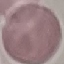 Malaria status: uninfected. Giemsa-stained preparation. Automatically extracted cell patch, resized to 64 × 64 pixels. Thin blood film. Photographed with a smartphone camera at the microscope eyepiece.